Locate and identify every blood parasite.
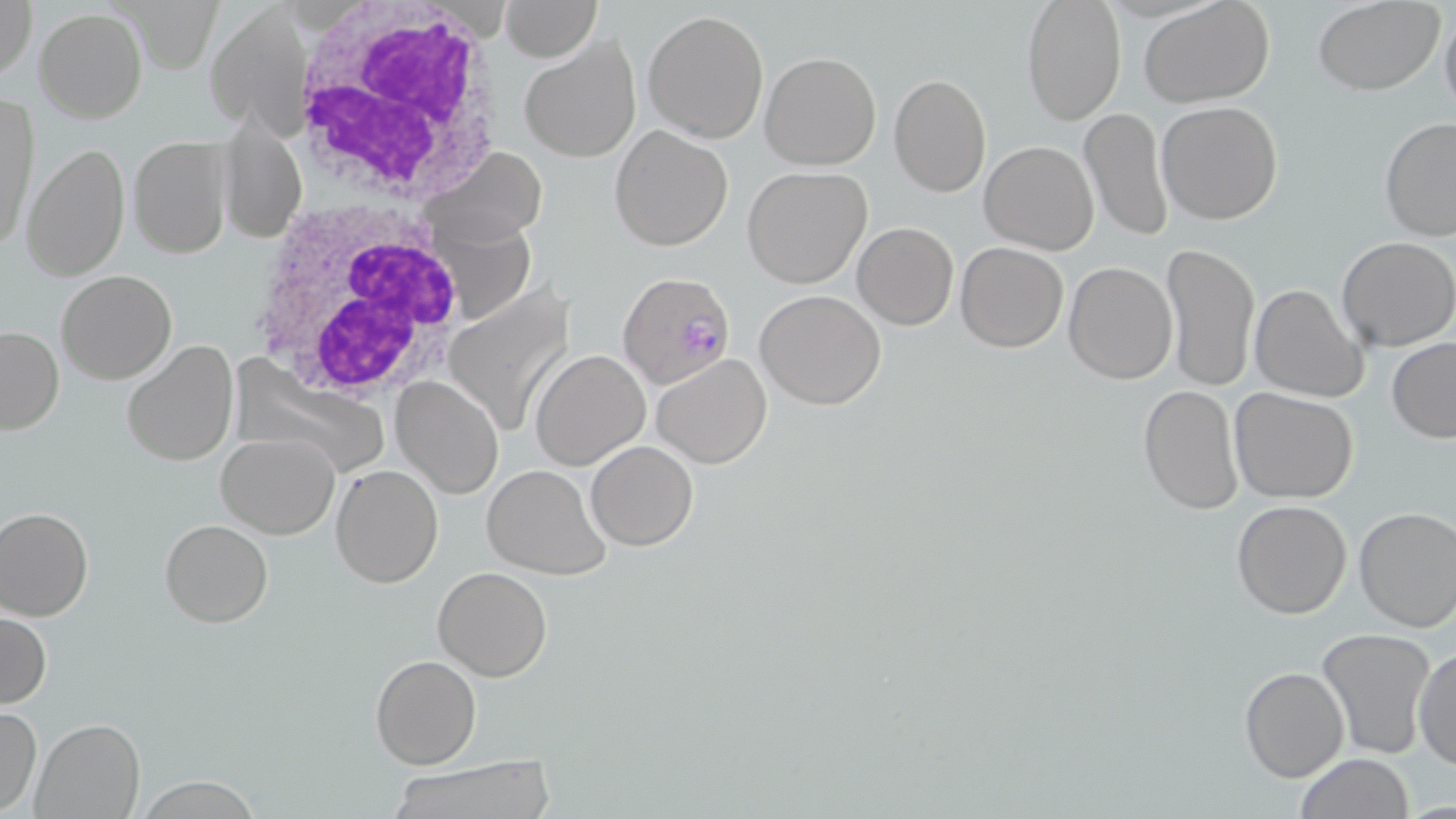
Approximate bounding boxes as (x1,y1)-(x2,y2) corner pairs in pixels.
Plasmodium falciparum-infected red blood cells: (618,271)-(734,389).
No Plasmodium ovale, Plasmodium malariae, Plasmodium vivax, Babesia divergens, or Trypanosoma brucei observed.

slide_level_diagnosis: Plasmodium falciparum
magnification: 1000x
modality: light microscopy
preparation: thin blood film
uninfected_red_blood_cell_locations: 'approximate bounding boxes as (x1,y1)-(x2,y2) corner pairs in pixels: (1,0)-(37,84), (499,0)-(600,62), (504,0)-(617,116), (1021,0)-(1126,126), (1138,0)-(1276,107), (1312,0)-(1446,95), (1439,3)-(1456,122), (35,7)-(148,123), (642,9)-(769,144), (210,10)-(311,132), (519,34)-(642,164), (759,52)-(883,170), (889,73)-(992,198), (1,97)-(35,254), (1156,101)-(1285,225), (1079,107)-(1175,243), (219,112)-(307,246), (1376,117)-(1456,243), (609,125)-(733,251), (128,135)-(233,259), (979,140)-(1100,254), (22,142)-(131,280), (420,144)-(547,248), (741,165)-(873,289), (456,210)-(550,322), (852,221)-(958,330), (1337,236)-(1455,351), (1161,241)-(1260,392), (955,242)-(1068,352), (1064,262)-(1178,384), (56,270)-(177,384), (448,271)-(580,432), (1249,283)-(1368,403), (756,290)-(887,410), (0,324)-(63,436), (120,338)-(239,467), (1387,338)-(1456,443), (529,348)-(650,470), (651,354)-(772,467), (231,362)-(391,480), (392,375)-(503,498), (1137,385)-(1244,517), (1228,386)-(1360,503), (216,432)-(339,538), (586,441)-(699,550), (481,462)-(612,579), (330,463)-(444,588), (1231,499)-(1354,620), (0,506)-(94,621), (1354,507)-(1455,632), (159,519)-(272,628), (431,566)-(555,682), (1,610)-(51,708), (1316,627)-(1437,760), (1414,645)-(1454,773), (370,654)-(481,768), (1239,666)-(1350,782), (0,704)-(42,814), (30,717)-(144,819), (1295,753)-(1417,819), (384,761)-(553,819), (131,777)-(265,816)'
image_size: 1456×819 pixels
white_blood_cell_locations: 'approximate bounding boxes as (x1,y1)-(x2,y2) corner pairs in pixels: (288,1)-(506,206), (244,200)-(470,405)'
stain: May-Grünwald-Giemsa
field_of_view: single